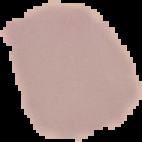
Summary:
  - Preparation: thin blood film
  - Result: negative for malaria parasites
  - Image size: 142×142 pixels
  - Image type: cell region segmented out of the field of view; surrounding area masked to black